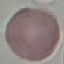

Malaria status: uninfected. Thin blood film. Automatically extracted cell patch, resized to 64 × 64 pixels. Acquired by smartphone through the microscope eyepiece. Giemsa-stained preparation.